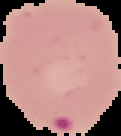
preparation: thin blood film
result: malaria parasites detected
image_type: cell region segmented out of the field of view; surrounding area masked to black
image_size: 121×136 pixels